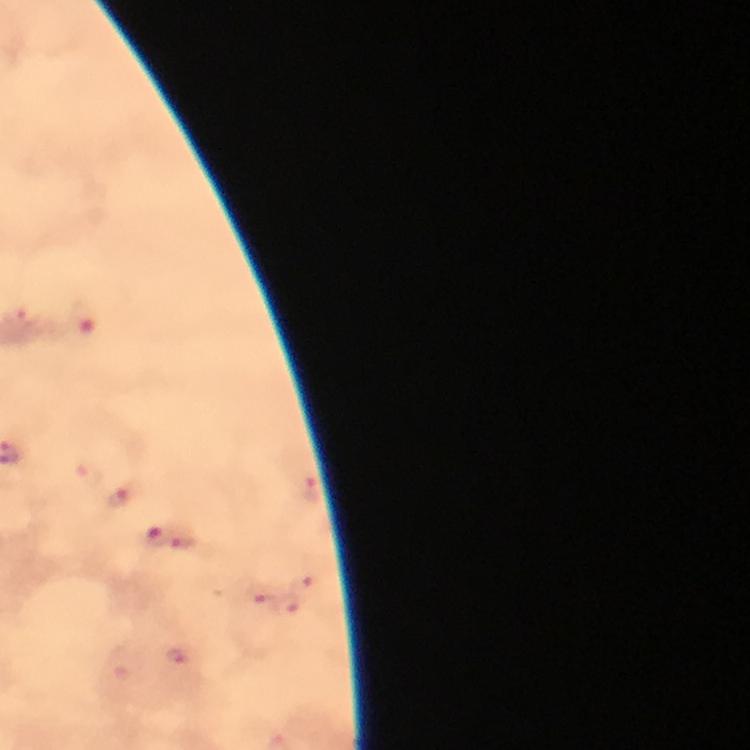

cropped from = a single field of view
malaria parasite locations = approximate centers as [x, y] in pixels: [85, 475], [310, 489], [123, 496], [156, 535], [183, 540], [308, 584], [267, 605], [294, 608], [178, 655]
immersion oil = applied
context = from a diagnostic examination for malaria
capture = smartphone photograph through a microscope
image size = 750×750 pixels
stain = Giemsa
preparation = thick blood film
magnification = 100x